Describe the morphology of the erythrocytes.
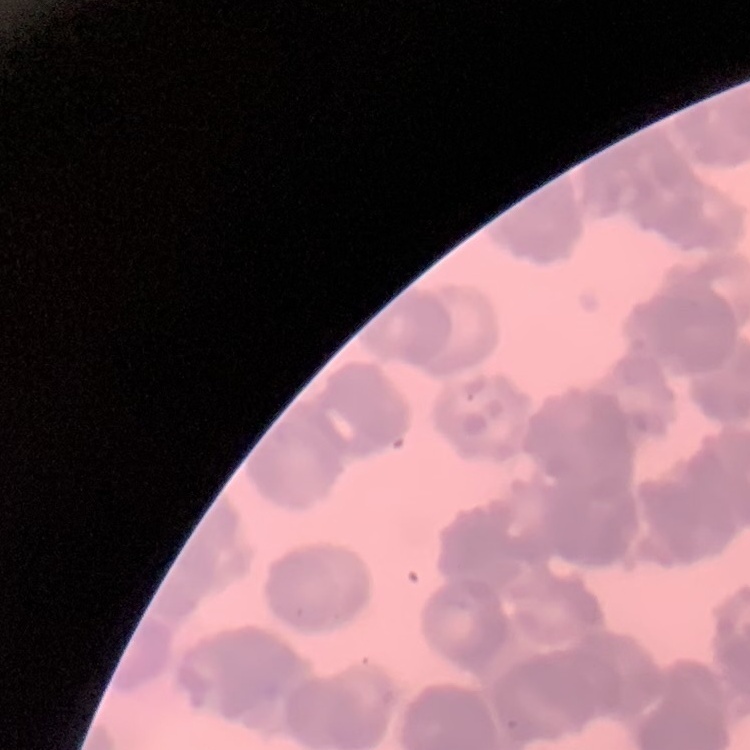

Rouleaux formation.

{
  "image_type": "square crop of a larger photomicrograph",
  "stain": "Field's or Giemsa",
  "preparation": "thin blood film"
}